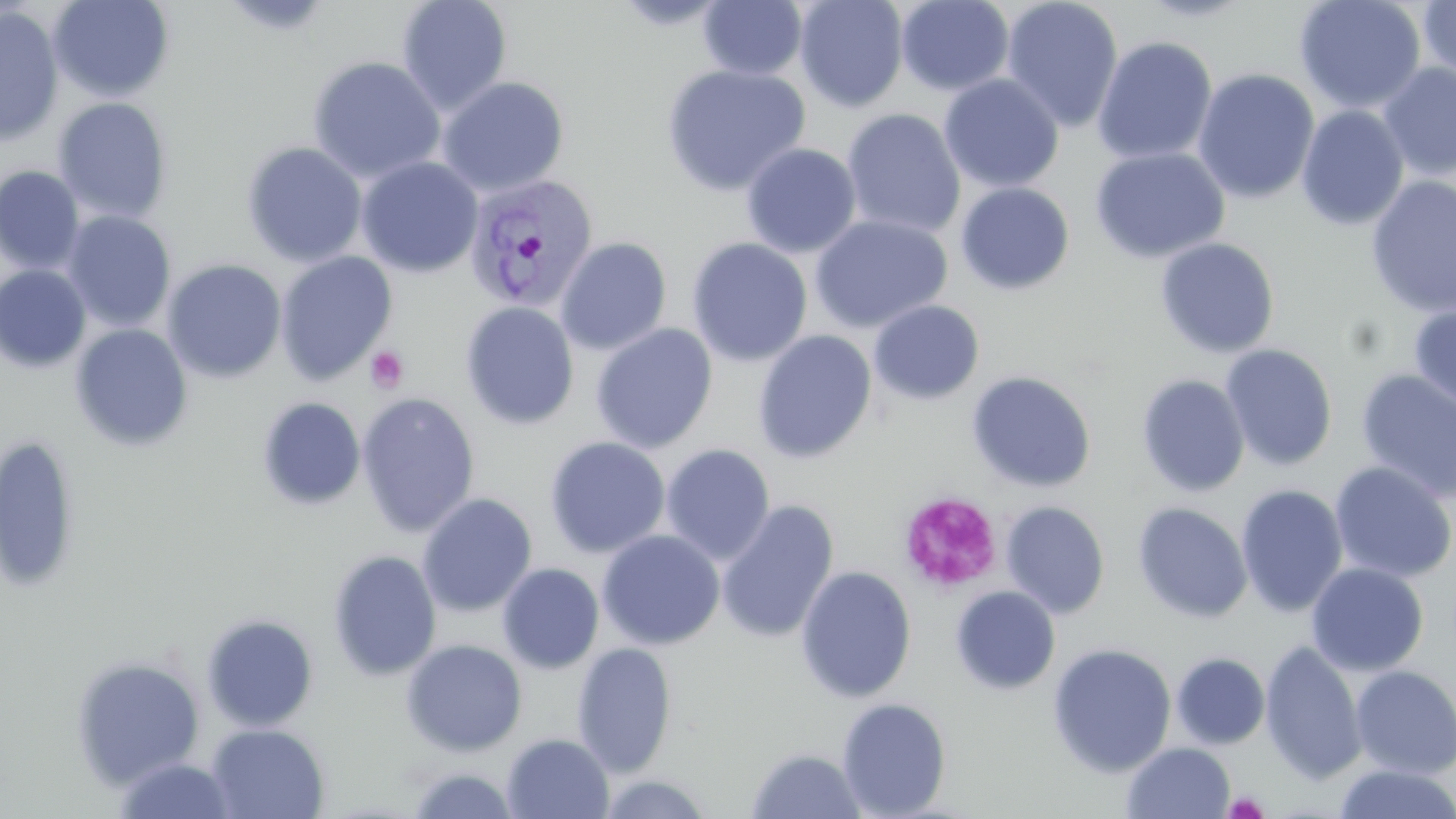

Summary:
  - Coordinate format: approximate bounding boxes as named x1/y1/x2/y2 corners in pixels
  - Plasmodium vivax-infected red blood cell locations: (x1=463, y1=173, x2=599, y2=313)
  - Uninfected red blood cell locations: (x1=48, y1=0, x2=175, y2=102), (x1=217, y1=0, x2=341, y2=37), (x1=396, y1=0, x2=512, y2=115), (x1=794, y1=0, x2=909, y2=112), (x1=1000, y1=0, x2=1123, y2=132), (x1=1135, y1=0, x2=1258, y2=23), (x1=1293, y1=0, x2=1427, y2=115), (x1=698, y1=1, x2=808, y2=80), (x1=895, y1=1, x2=1015, y2=96), (x1=1418, y1=2, x2=1456, y2=81), (x1=0, y1=7, x2=64, y2=146), (x1=1092, y1=36, x2=1217, y2=165), (x1=307, y1=56, x2=446, y2=183), (x1=1377, y1=63, x2=1456, y2=180), (x1=660, y1=64, x2=810, y2=197), (x1=1192, y1=67, x2=1320, y2=204), (x1=938, y1=74, x2=1065, y2=193), (x1=436, y1=76, x2=570, y2=197), (x1=53, y1=97, x2=174, y2=224), (x1=1296, y1=105, x2=1410, y2=231), (x1=841, y1=108, x2=966, y2=239), (x1=241, y1=141, x2=367, y2=267), (x1=741, y1=142, x2=862, y2=258), (x1=1090, y1=146, x2=1230, y2=264), (x1=356, y1=156, x2=483, y2=278), (x1=0, y1=166, x2=84, y2=275), (x1=1365, y1=175, x2=1456, y2=318), (x1=954, y1=182, x2=1075, y2=296), (x1=62, y1=211, x2=176, y2=332), (x1=809, y1=215, x2=952, y2=333), (x1=555, y1=236, x2=672, y2=355), (x1=686, y1=237, x2=812, y2=367), (x1=1155, y1=237, x2=1280, y2=358), (x1=275, y1=251, x2=397, y2=385), (x1=162, y1=259, x2=286, y2=384), (x1=0, y1=264, x2=91, y2=373), (x1=868, y1=299, x2=985, y2=405), (x1=460, y1=302, x2=580, y2=431), (x1=1407, y1=303, x2=1456, y2=415), (x1=70, y1=324, x2=193, y2=451), (x1=590, y1=324, x2=718, y2=454), (x1=753, y1=330, x2=877, y2=463), (x1=1220, y1=343, x2=1339, y2=471), (x1=1355, y1=369, x2=1456, y2=504), (x1=966, y1=370, x2=1097, y2=493), (x1=1136, y1=373, x2=1250, y2=498), (x1=357, y1=392, x2=480, y2=537), (x1=257, y1=396, x2=366, y2=511), (x1=0, y1=433, x2=82, y2=595), (x1=544, y1=436, x2=670, y2=558), (x1=660, y1=443, x2=776, y2=564), (x1=1329, y1=460, x2=1456, y2=584), (x1=1235, y1=484, x2=1348, y2=617), (x1=417, y1=493, x2=538, y2=617), (x1=716, y1=499, x2=839, y2=643), (x1=1000, y1=500, x2=1110, y2=619), (x1=1132, y1=501, x2=1252, y2=623), (x1=596, y1=529, x2=725, y2=651), (x1=328, y1=550, x2=442, y2=681), (x1=1305, y1=562, x2=1429, y2=676), (x1=497, y1=563, x2=604, y2=674), (x1=795, y1=565, x2=917, y2=704), (x1=950, y1=585, x2=1060, y2=695), (x1=201, y1=613, x2=319, y2=731), (x1=401, y1=639, x2=527, y2=756), (x1=1259, y1=640, x2=1367, y2=784), (x1=571, y1=641, x2=678, y2=778), (x1=1047, y1=642, x2=1177, y2=777), (x1=1170, y1=652, x2=1270, y2=750), (x1=69, y1=655, x2=206, y2=790), (x1=1350, y1=664, x2=1456, y2=779), (x1=837, y1=697, x2=952, y2=818), (x1=205, y1=723, x2=330, y2=819), (x1=502, y1=733, x2=613, y2=818), (x1=1123, y1=742, x2=1235, y2=819), (x1=745, y1=747, x2=868, y2=818), (x1=110, y1=755, x2=241, y2=818), (x1=1333, y1=764, x2=1456, y2=819), (x1=404, y1=765, x2=524, y2=818), (x1=594, y1=773, x2=717, y2=818)
  - Platelet locations: (x1=365, y1=346, x2=409, y2=394), (x1=899, y1=490, x2=1003, y2=594), (x1=1223, y1=791, x2=1270, y2=818)
  - Slide-level diagnosis: Plasmodium vivax
  - Stain: May-Grünwald-Giemsa
  - Modality: light microscopy
  - Field of view: one of a larger specimen
  - Preparation: thin blood smear
  - Image size: 1456×819 pixels
  - Magnification: 1000x